Classify this cell by malaria status.
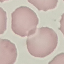
Uninfected.

capture = smartphone through the microscope eyepiece
preparation = thin blood smear
stain = Giemsa
image type = cell patch, automatically extracted from a larger field of view and resized to 64 × 64 pixels